Name the parasite shown.
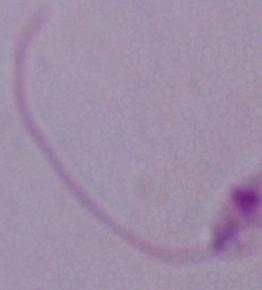

Leishmania.

{
  "magnification": "1000x",
  "modality": "micrograph"
}